Locate and identify every blood parasite.
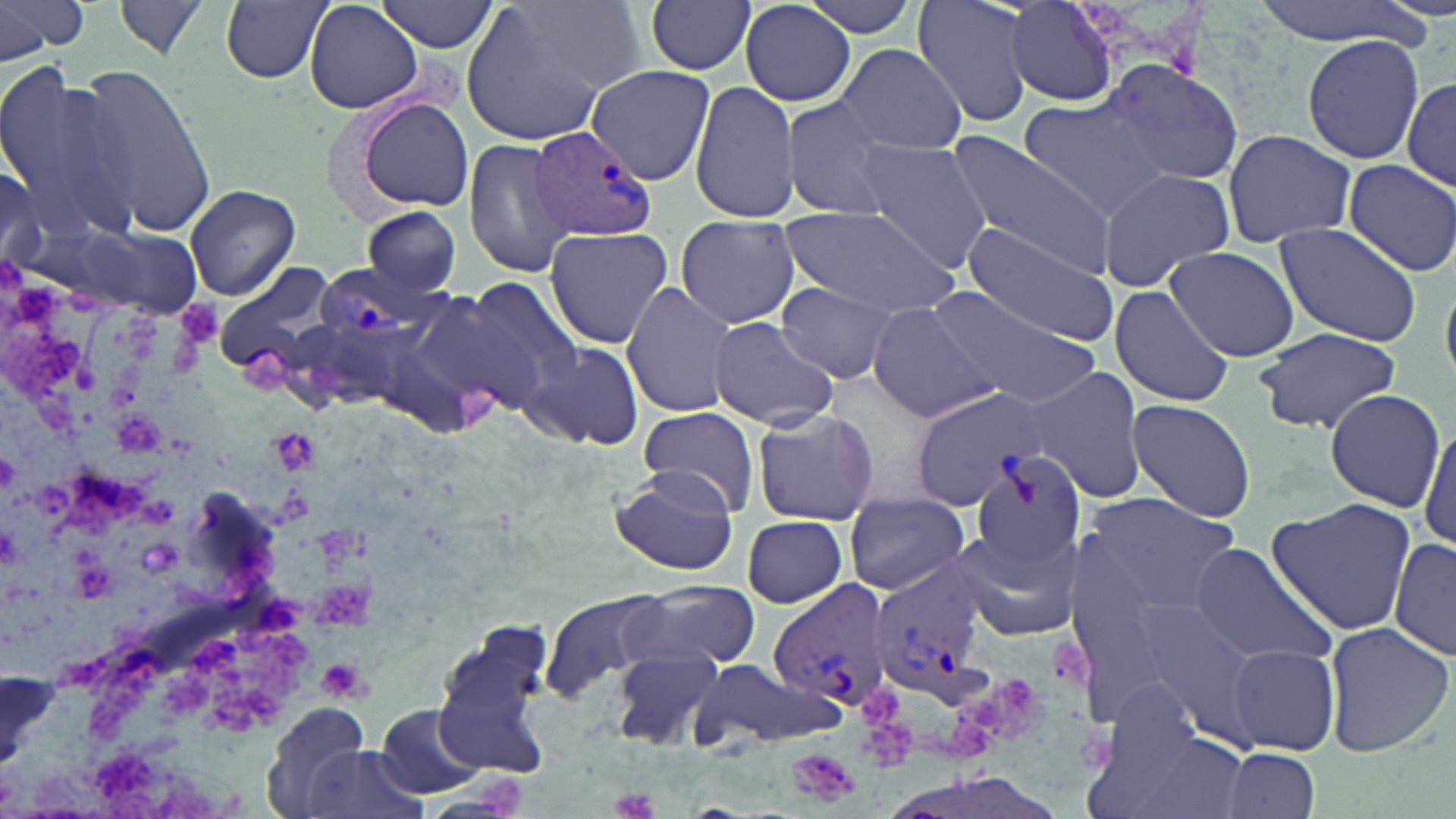
Approximate bounding boxes as (x1,y1)-(x2,y2) corner pairs in pixels.
Plasmodium vivax-infected red blood cells: (527,123)-(657,244), (310,262)-(434,343), (867,560)-(992,702), (766,581)-(893,714).
No Plasmodium falciparum, Plasmodium ovale, Plasmodium malariae, Babesia divergens, or Trypanosoma brucei observed.

slide-level diagnosis = Plasmodium vivax
modality = optical microscopy
uninfected red blood cell locations = approximate bounding boxes as (x1,y1)-(x2,y2) corner pairs in pixels: (0,0)-(88,62), (378,0)-(504,53), (644,0)-(756,76), (796,0)-(923,39), (914,0)-(1036,129), (1250,0)-(1432,46), (112,1)-(211,60), (220,1)-(332,84), (304,1)-(424,114), (1004,1)-(1118,108), (740,2)-(858,108), (460,3)-(620,146), (1301,32)-(1425,167), (834,42)-(966,157), (1095,59)-(1246,185), (0,63)-(129,230), (586,63)-(716,185), (67,65)-(217,231), (1401,77)-(1456,193), (689,81)-(797,223), (781,97)-(899,222), (350,98)-(475,213), (1016,100)-(1163,219), (1222,128)-(1356,247), (463,135)-(578,278), (850,137)-(994,273), (945,137)-(1117,273), (1342,160)-(1456,276), (1096,168)-(1234,288), (1,169)-(42,273), (185,184)-(302,299), (360,204)-(463,296), (780,204)-(958,316), (675,214)-(802,330), (958,222)-(1123,343), (1274,222)-(1424,348), (72,223)-(202,319), (544,227)-(672,349), (1165,246)-(1299,361), (213,263)-(338,374), (457,275)-(586,400), (621,281)-(735,418), (774,281)-(906,384), (926,284)-(1102,409), (1108,286)-(1236,407), (403,289)-(533,418), (865,303)-(996,423), (705,318)-(839,429), (1252,327)-(1404,434), (374,334)-(482,438), (524,342)-(644,450), (1023,366)-(1148,503), (910,384)-(1043,510), (1323,386)-(1446,511), (1127,397)-(1256,522), (635,406)-(760,517), (749,408)-(880,527), (1417,419)-(1455,556), (970,450)-(1087,567), (608,466)-(738,576), (845,491)-(969,597), (1076,493)-(1248,624), (1266,498)-(1418,637), (742,515)-(849,607), (947,525)-(1083,641), (1391,539)-(1454,662), (1186,542)-(1338,669), (633,582)-(762,669), (541,588)-(674,701), (1124,600)-(1267,742), (433,619)-(560,774), (1321,621)-(1454,760), (1227,645)-(1339,753), (610,647)-(728,749), (316,656)-(372,702), (689,662)-(845,750), (260,701)-(371,818), (373,704)-(484,797), (1095,721)-(1246,819), (303,745)-(429,819), (1222,747)-(1322,819)
image size = 1456×819 pixels
stain = May-Grünwald-Giemsa
platelet locations = approximate bounding boxes as (x1,y1)-(x2,y2) corner pairs in pixels: (315,659)-(367,698), (786,749)-(860,805), (610,788)-(658,819)
preparation = thin blood film
magnification = 1000x
field of view = single